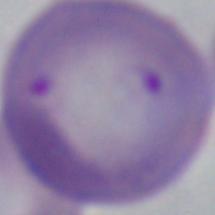
A Babesia parasite is shown. Photomicrograph. 1000x magnification.